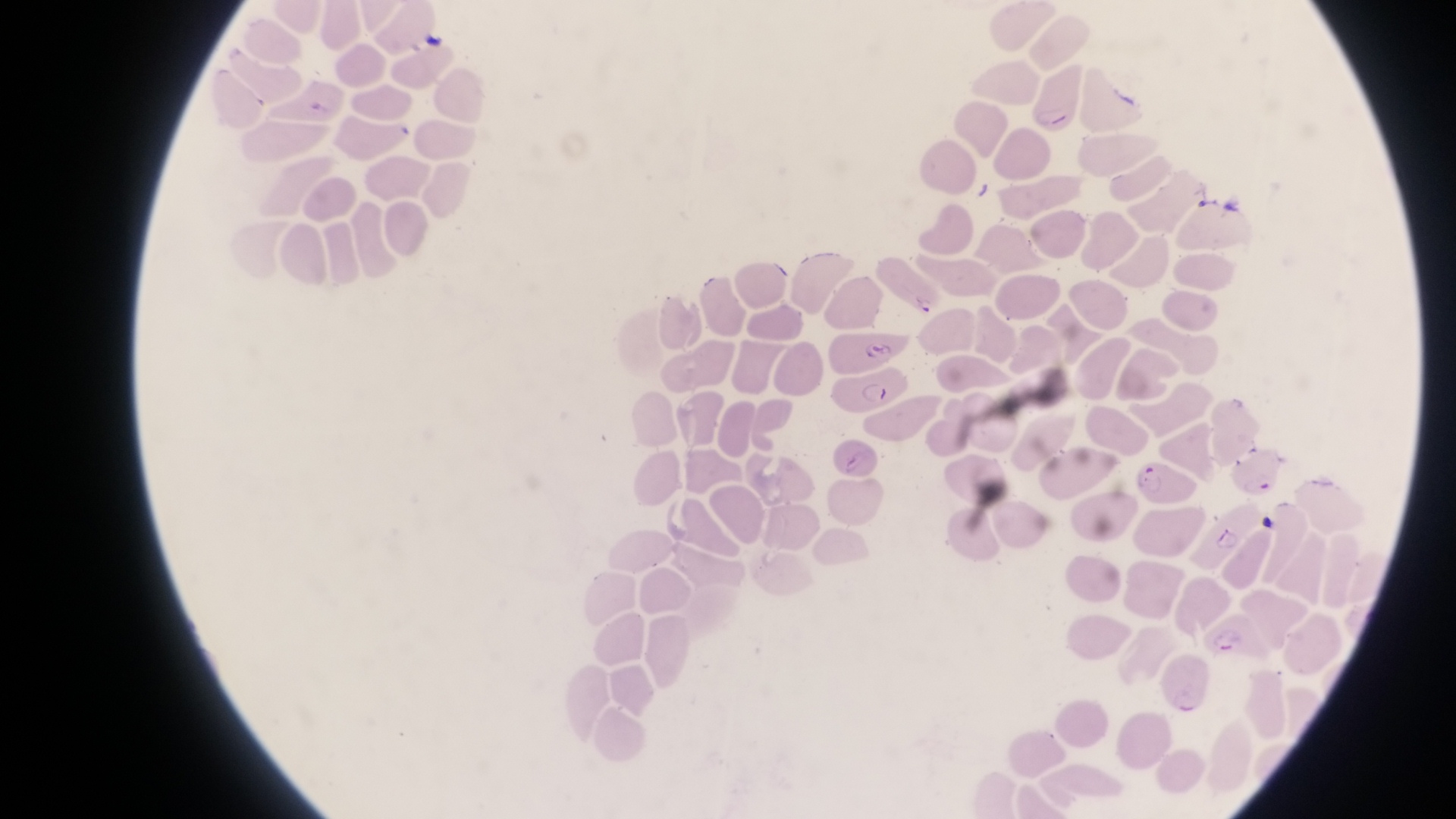

trophozoite locations = approximate bounding boxes as (left, top, right, bottom) in pixels: (911, 293, 943, 319)
image size = 1456×819 pixels
artifact (platelet-like body, stain precipitate, or debris) locations = approximate bounding boxes as (left, top, right, bottom) in pixels: (415, 27, 449, 60), (307, 92, 333, 124), (971, 180, 998, 207), (1222, 188, 1245, 218)
preparation = thin blood smear
magnification = 1000x
parasitised red blood cell locations = approximate bounding boxes as (left, top, right, bottom) in pixels: (1031, 64, 1083, 137), (840, 370, 903, 420), (832, 442, 884, 479), (1231, 446, 1284, 499), (1136, 455, 1196, 511), (1194, 525, 1249, 564), (1207, 611, 1263, 664), (1160, 644, 1209, 716)
country = Uganda
field of view = single
capture = smartphone photograph through the eyepiece of an Olympus CX-23 microscope